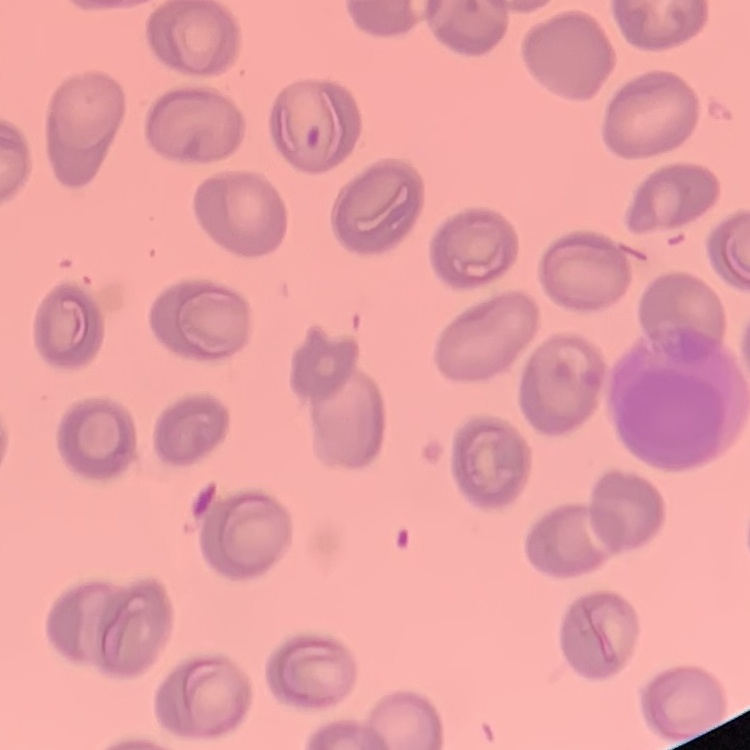
Summary:
  - Red blood cell morphology: no rouleaux formation
  - Image type: one tile cut from a larger photomicrograph
  - Preparation: thin peripheral smear
  - Stain: Field's or Giemsa